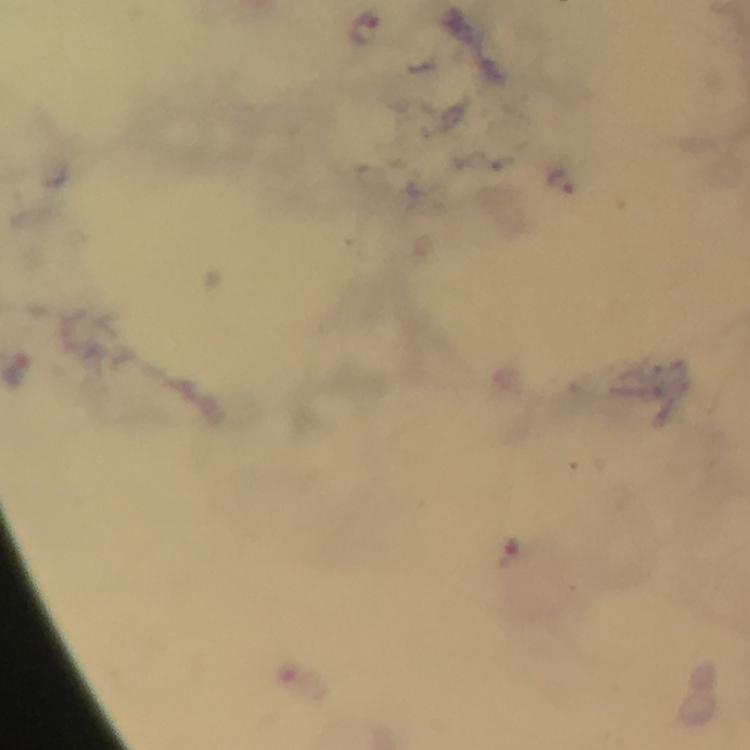 Approximate centers as [x, y] in pixels. Malaria parasite locations: [360, 26], [559, 179]. Thick blood smear. Giemsa stain. Image is 750×750 pixels. From a diagnostic examination for malaria. Smartphone photograph taken through a microscope. Cropped region of a single field of view. At 100x magnification. Immersion oil was used.